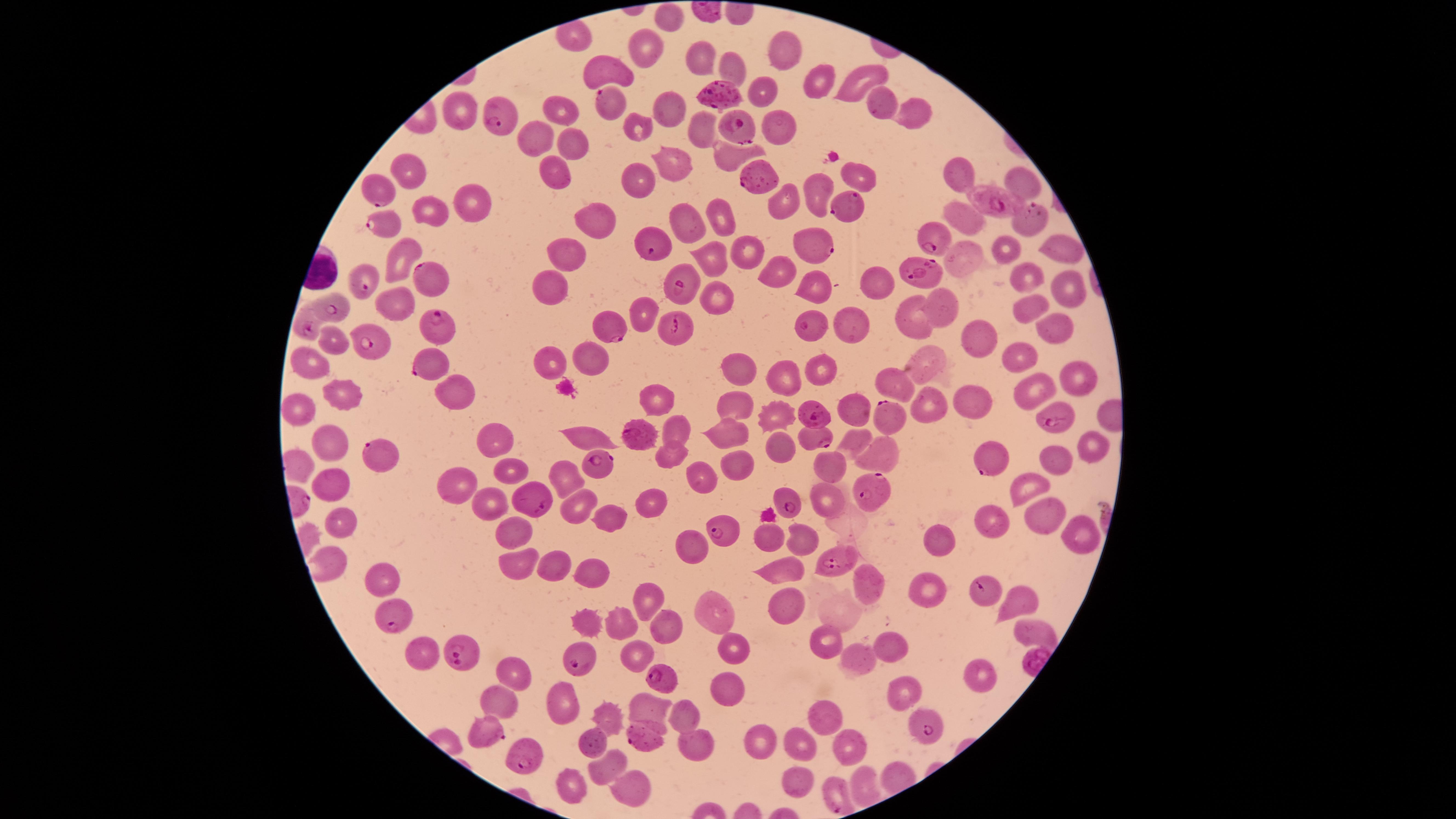
Approximate marker points as [x, y] in pixels. WBCs: [312, 271]. Uninfected RBCs: [669, 20], [645, 47], [782, 53], [706, 58], [733, 59], [611, 68], [820, 74], [861, 80], [761, 94], [871, 101], [457, 107], [668, 110], [914, 111], [560, 112], [782, 124], [635, 127], [700, 130], [540, 143], [569, 143], [670, 154], [732, 154], [412, 165], [860, 172], [557, 176], [957, 176], [1026, 180], [643, 183], [822, 187], [785, 197], [467, 201], [431, 206], [591, 212], [719, 214], [960, 216], [691, 221], [1061, 247], [749, 249], [399, 250], [965, 251], [1007, 252], [717, 254], [571, 255], [771, 267], [1025, 272], [877, 279], [816, 281], [556, 286], [1066, 288], [720, 295], [401, 301], [947, 306], [647, 308], [1022, 308], [918, 318], [855, 323], [1050, 324], [983, 337], [335, 343], [591, 355], [925, 358], [314, 359], [551, 361], [1019, 361], [739, 367], [825, 369], [786, 372], [1080, 373], [887, 377], [452, 388], [1040, 388], [344, 393], [657, 399], [739, 399], [297, 401], [938, 404], [975, 407], [856, 409], [777, 412], [676, 428], [732, 433], [495, 434], [588, 434], [861, 439], [329, 443], [781, 443], [1091, 443], [881, 449], [666, 450], [1052, 456], [512, 458], [731, 460], [830, 470], [563, 473], [699, 475], [327, 478], [457, 482], [1021, 484], [487, 496], [576, 496], [825, 496], [646, 500], [1039, 508], [340, 513], [614, 517], [990, 519], [517, 530], [1078, 532], [772, 537], [804, 537], [941, 537], [695, 543], [518, 560], [549, 562], [329, 564], [590, 569], [779, 571], [375, 578], [872, 580], [929, 586], [648, 588], [1018, 598], [788, 604], [707, 609], [586, 620], [617, 623], [665, 624], [1035, 634], [826, 644], [730, 645], [420, 648], [638, 649], [896, 649], [860, 654], [512, 668], [981, 670], [730, 691], [898, 692], [503, 696], [566, 698], [650, 708], [601, 713], [686, 715], [825, 715], [753, 733], [594, 739], [695, 740], [806, 746], [854, 746], [610, 760], [797, 779], [638, 784], [575, 786]. Parasitized RBCs: [714, 86], [610, 105], [495, 113], [729, 121], [751, 177], [382, 189], [994, 201], [843, 204], [1031, 215], [379, 217], [927, 236], [654, 239], [810, 244], [425, 269], [921, 272], [364, 279], [674, 280], [333, 302], [434, 323], [609, 323], [671, 323], [806, 323], [306, 325], [375, 343], [425, 368], [814, 411], [1053, 413], [887, 415], [641, 432], [816, 439], [376, 453], [986, 457], [591, 462], [870, 489], [534, 496], [785, 500], [726, 527], [828, 557], [985, 594], [394, 617], [463, 649], [579, 652], [661, 677], [922, 724], [497, 736], [642, 738], [523, 756], [838, 787]. Species: Plasmodium falciparum. Single field of view. Image is 1456×819 pixels. Presence: malaria parasites identified. The visible region is circular. Thin smear of blood. Giemsa stain. Smartphone photograph through the microscope eyepiece.